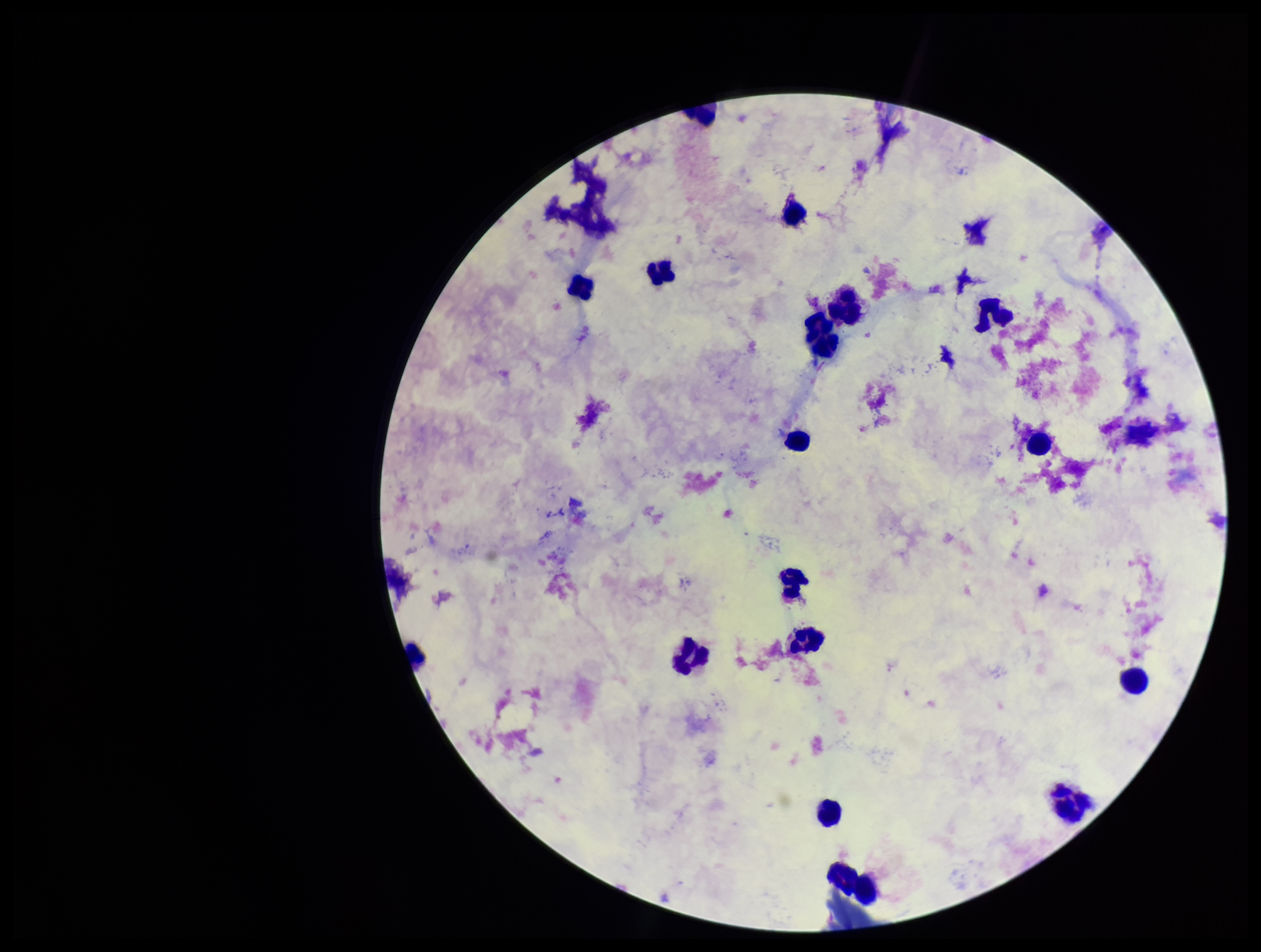

Image is 1261×952 pixels. Photographed through the microscope eyepiece with a smartphone camera. Parasite count: 0. Plasmodium parasites: none detected. Leukocyte count: 18. Preparation: thick smear. Single field of view. Giemsa stain. Patient malaria status: negative.